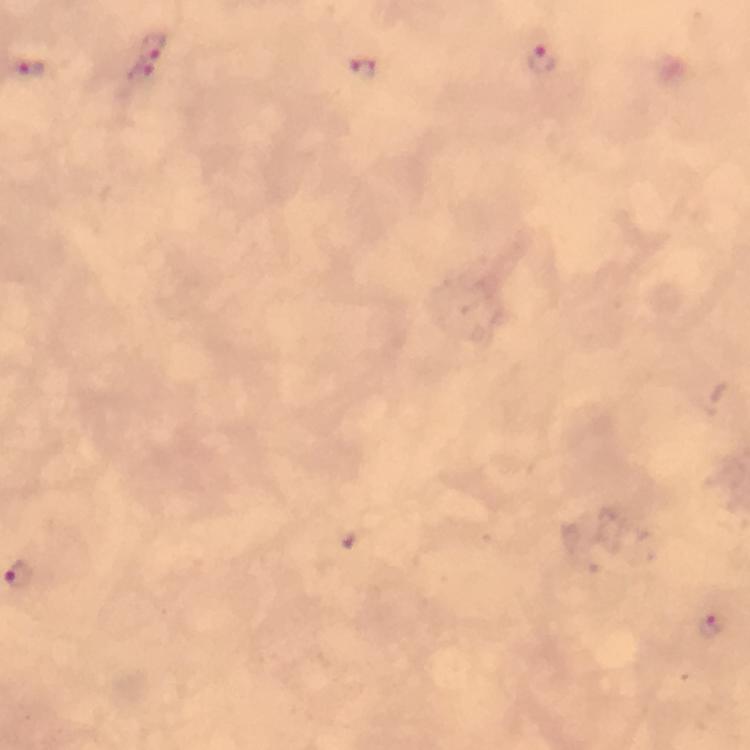
Approximate centers as {x, y} in pixels.
Summary:
  - Plasmodium parasite locations: {152, 42}, {545, 61}, {364, 67}, {140, 74}, {709, 625}
  - Immersion oil: applied
  - Magnification: 100x
  - Preparation: thick smear
  - Cropped from: a single field of view
  - Image size: 750×750 pixels
  - Context: from a malaria diagnostic workup
  - Stain: Giemsa
  - Capture: smartphone camera through the microscope